Assess this cell for malaria.
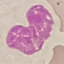

It is uninfected.

Summary:
  - Preparation: thin blood film
  - Capture: smartphone camera at the microscope eyepiece
  - Image type: cell patch, automatically extracted from a larger field of view and resized to 64 × 64 pixels
  - Stain: Giemsa